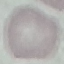
result = negative for malaria parasites
capture = smartphone camera at the microscope eyepiece
preparation = thin blood smear
image type = automatically extracted cell patch, resized to 64 × 64 pixels
stain = Giemsa